Describe the morphology of the red blood cells.
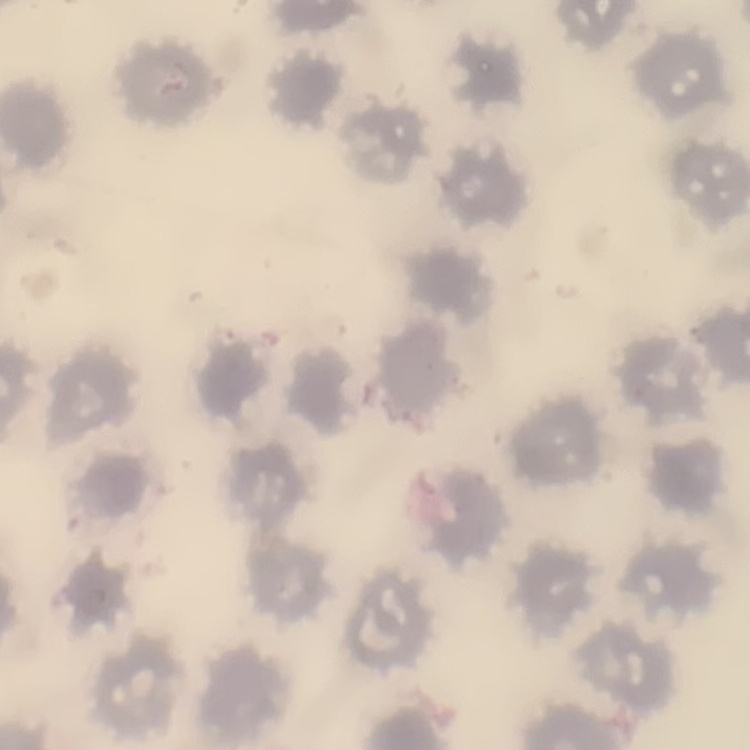
No rouleaux formation.

preparation: thin peripheral smear
image_type: one tile cut from a larger photomicrograph
stain: Field's or Giemsa